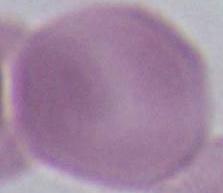

identification = erythrocyte
modality = micrograph
magnification = 1000x